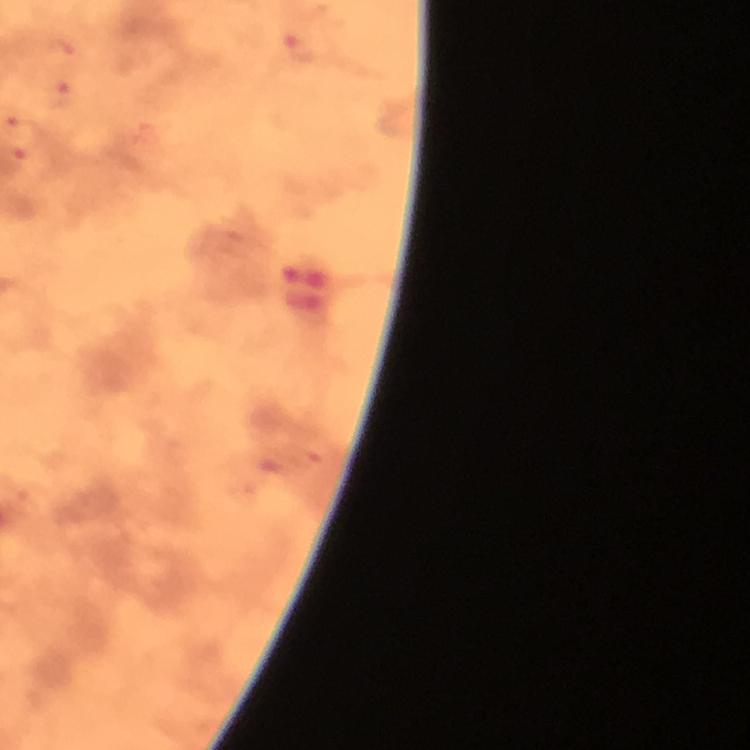
magnification = 100x
context = from a diagnostic examination for malaria
immersion oil = applied
cropped from = a single field of view
Plasmodium parasite locations = approximate centers as (x, y) in pixels: (301, 45), (63, 51), (59, 93)
stain = Giemsa
preparation = thick blood film
image size = 750×750 pixels
capture = smartphone camera through the microscope